Locate and identify every blood parasite.
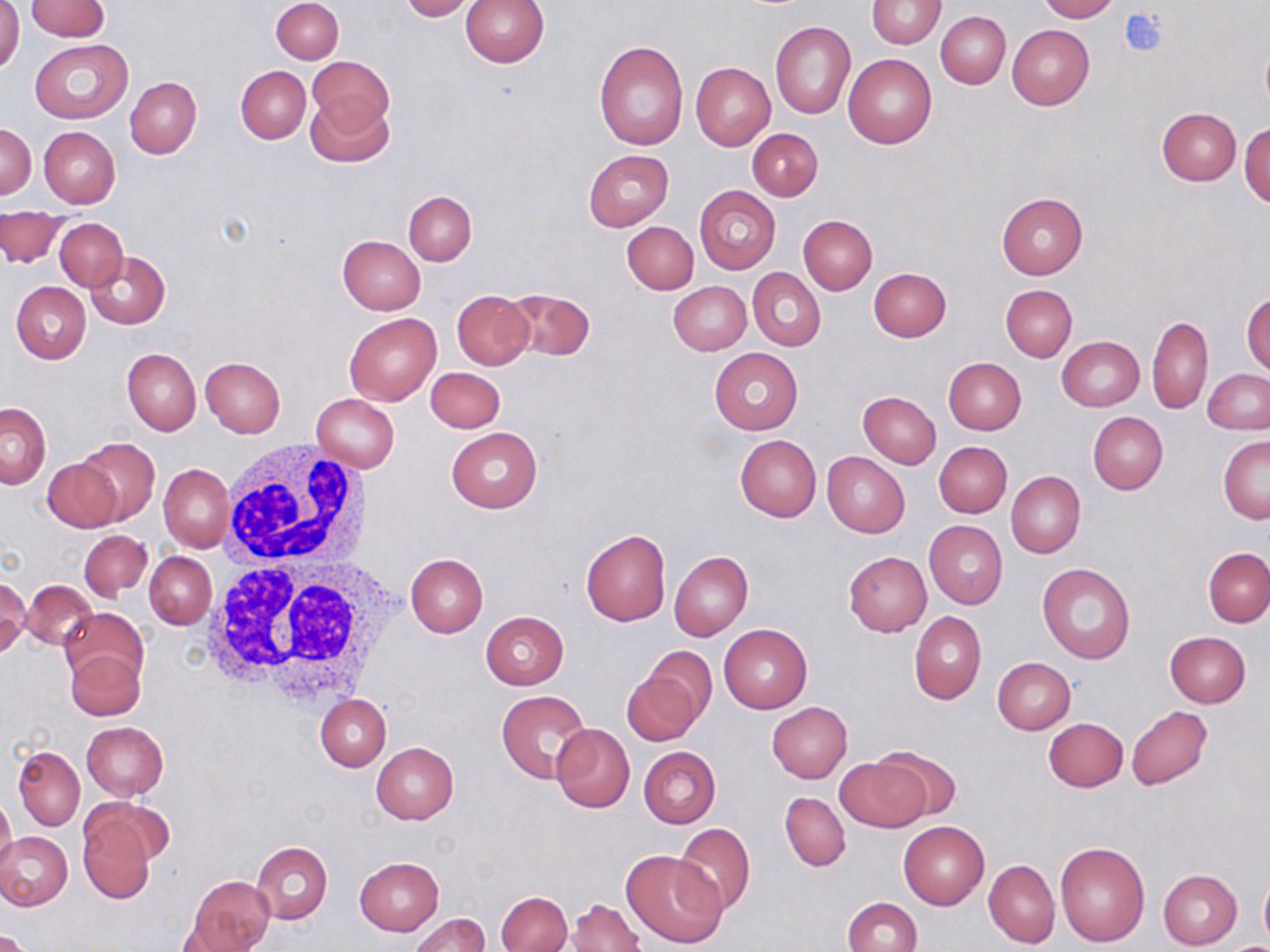
No blood parasites seen.

{
  "slide_level_diagnosis": "negative for blood parasites",
  "preparation": "thin blood smear",
  "stain": "May-Grünwald-Giemsa",
  "white_blood_cell_locations": "approximate bounding boxes as [x1, y1, x2, y2] in pixels: [215, 446, 382, 584], [194, 522, 409, 709]",
  "platelet_locations": "approximate bounding boxes as [x1, y1, x2, y2] in pixels: [1119, 7, 1168, 57]",
  "field_of_view": "one of a larger specimen",
  "uninfected_red_blood_cell_locations": "approximate bounding boxes as [x1, y1, x2, y2] in pixels: [25, 0, 109, 40], [271, 0, 343, 62], [399, 0, 476, 21], [460, 0, 549, 69], [867, 0, 945, 48], [1038, 0, 1117, 22], [0, 2, 23, 76], [936, 12, 1010, 88], [770, 20, 855, 119], [1007, 24, 1093, 110], [1260, 38, 1270, 115], [30, 39, 132, 122], [594, 40, 688, 150], [844, 53, 937, 148], [309, 56, 393, 135], [691, 62, 775, 150], [236, 66, 311, 143], [126, 77, 201, 159], [305, 93, 393, 167], [1156, 107, 1242, 184], [1, 122, 37, 201], [1240, 122, 1269, 207], [38, 126, 121, 208], [748, 127, 823, 200], [584, 149, 673, 231], [694, 185, 781, 273], [403, 190, 476, 265], [996, 191, 1088, 279], [0, 209, 64, 267], [798, 215, 877, 294], [55, 218, 128, 291], [622, 222, 698, 294], [337, 235, 425, 314], [87, 252, 170, 329], [749, 268, 826, 351], [868, 268, 950, 342], [668, 281, 750, 355], [11, 282, 90, 364], [1001, 284, 1077, 361], [503, 288, 595, 360], [451, 289, 533, 369], [1242, 292, 1270, 375], [345, 312, 440, 406], [1147, 315, 1213, 414], [1056, 337, 1144, 411], [710, 348, 803, 434], [122, 349, 201, 435], [200, 357, 285, 439], [943, 357, 1026, 435], [426, 367, 505, 433], [1202, 368, 1270, 435], [858, 392, 940, 469], [311, 394, 399, 472], [1, 403, 50, 487], [1088, 412, 1167, 495], [447, 428, 542, 513], [735, 434, 821, 521], [1219, 435, 1269, 523], [77, 437, 158, 522], [933, 441, 1011, 517], [822, 452, 909, 538], [44, 457, 126, 531], [159, 464, 234, 553], [1006, 471, 1085, 558], [924, 521, 1006, 609], [580, 528, 671, 626], [78, 530, 152, 601], [1203, 546, 1270, 627], [669, 551, 752, 641], [843, 552, 931, 636], [145, 553, 216, 629], [406, 554, 488, 637], [1036, 562, 1135, 664], [0, 577, 31, 655], [22, 580, 96, 651], [60, 608, 149, 690], [480, 610, 569, 690], [909, 612, 987, 704], [718, 624, 811, 714], [1165, 632, 1250, 708], [643, 646, 718, 730], [65, 648, 146, 721], [993, 657, 1076, 733], [622, 668, 705, 747], [496, 689, 592, 785], [316, 694, 391, 771], [767, 701, 853, 782], [1126, 706, 1212, 789], [1043, 718, 1127, 791], [82, 721, 168, 800], [550, 722, 634, 813], [371, 742, 459, 824], [869, 746, 963, 823], [13, 747, 85, 830], [638, 747, 720, 828], [835, 756, 931, 833], [780, 792, 850, 871], [0, 796, 16, 874], [85, 798, 174, 871], [76, 810, 156, 903], [898, 820, 989, 909], [672, 823, 757, 917], [0, 832, 73, 911], [1055, 840, 1151, 947], [251, 842, 332, 923], [621, 850, 727, 948], [354, 856, 444, 936], [983, 859, 1060, 949], [1158, 869, 1243, 949], [1258, 870, 1270, 945], [186, 875, 276, 951], [498, 891, 571, 952], [566, 897, 644, 951], [843, 897, 922, 952], [407, 913, 489, 952], [1, 928, 33, 952], [1218, 940, 1270, 951]",
  "magnification": "1000x",
  "modality": "light microscopy",
  "image_size": "1270×952 pixels"
}